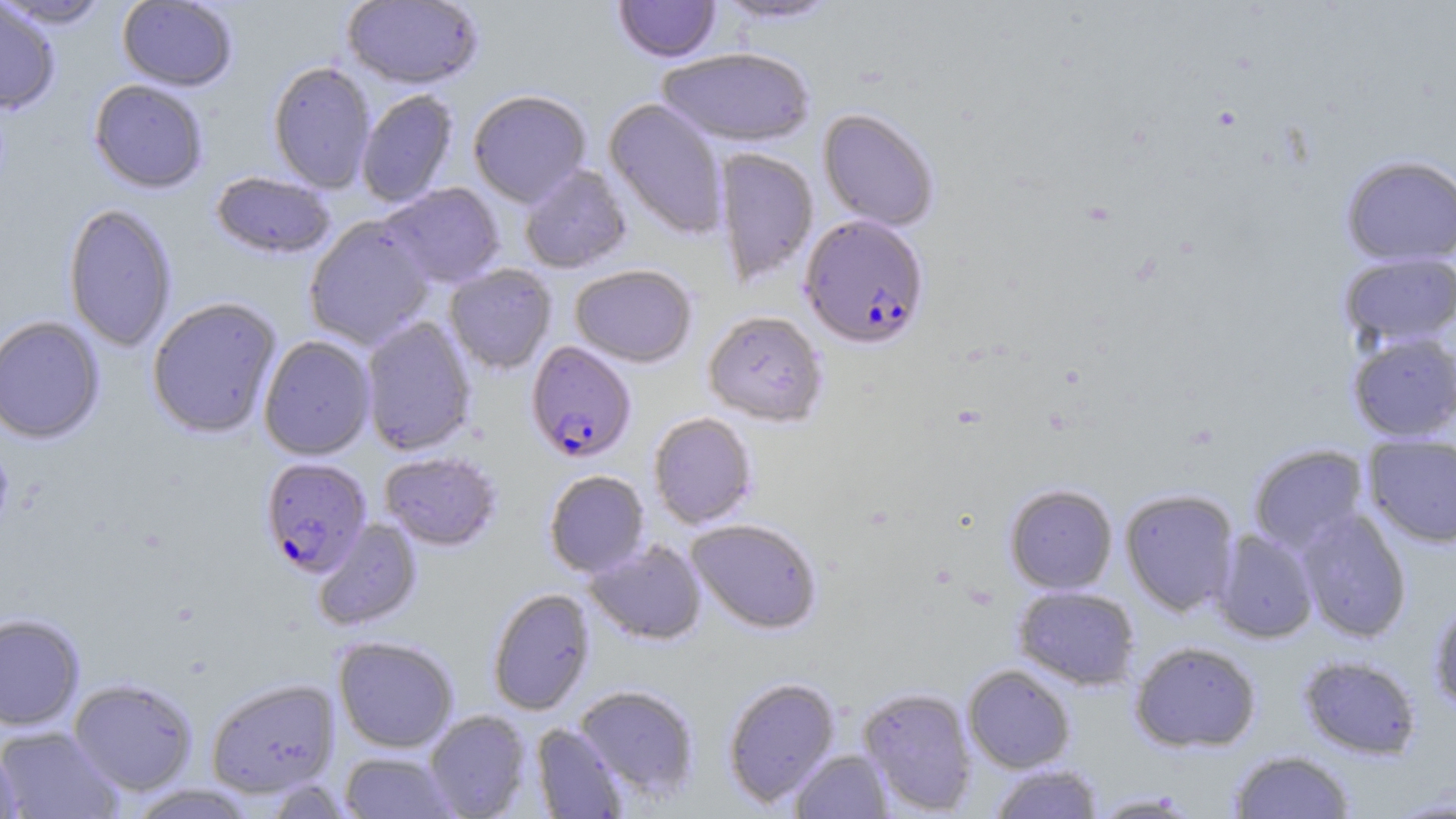
slide-level diagnosis = Plasmodium falciparum
magnification = 1000x
uninfected red blood cell locations = approximate bounding boxes as (x1,y1)-(x2,y2) corner pairs in pixels: (0,0)-(61,114), (342,0)-(484,90), (614,0)-(721,63), (714,0)-(843,27), (0,1)-(112,29), (117,1)-(237,91), (657,49)-(815,148), (267,61)-(376,194), (89,79)-(208,194), (356,90)-(459,208), (468,91)-(591,207), (604,98)-(729,240), (818,108)-(939,231), (713,148)-(818,287), (1340,154)-(1456,267), (519,165)-(632,274), (211,172)-(336,260), (380,183)-(505,289), (62,203)-(178,352), (303,217)-(435,350), (1339,252)-(1456,348), (444,264)-(557,375), (570,265)-(697,368), (146,297)-(282,439), (703,310)-(828,428), (0,316)-(106,445), (360,316)-(476,456), (1347,331)-(1456,442), (258,335)-(376,460), (648,412)-(758,529), (1363,434)-(1456,547), (1247,444)-(1370,553), (379,452)-(502,551), (544,470)-(649,578), (1004,484)-(1118,594), (1120,488)-(1240,617), (1296,509)-(1412,643), (312,518)-(423,631), (687,518)-(823,634), (1211,528)-(1319,643), (585,539)-(707,646), (1014,585)-(1140,690), (487,588)-(595,715), (1429,597)-(1456,713), (0,613)-(85,732), (333,637)-(458,753), (1130,640)-(1262,753), (1298,655)-(1421,759), (962,664)-(1075,773), (722,677)-(840,807), (69,678)-(198,796), (205,678)-(340,798), (574,685)-(700,803), (857,686)-(978,814), (424,710)-(532,818), (531,723)-(628,818), (0,726)-(124,818), (0,739)-(21,819), (790,748)-(893,818), (1228,750)-(1355,818), (339,751)-(458,818), (988,763)-(1104,819), (126,784)-(258,818), (1089,791)-(1203,817)
image size = 1456×819 pixels
Plasmodium falciparum-infected red blood cell locations = approximate bounding boxes as (x1,y1)-(x2,y2) corner pairs in pixels: (800,215)-(929,349), (526,341)-(636,464), (260,458)-(372,577)
field of view = one of a larger specimen
preparation = thin blood film
modality = optical microscopy
stain = May-Grünwald-Giemsa